Outline each blood parasite and name the species.
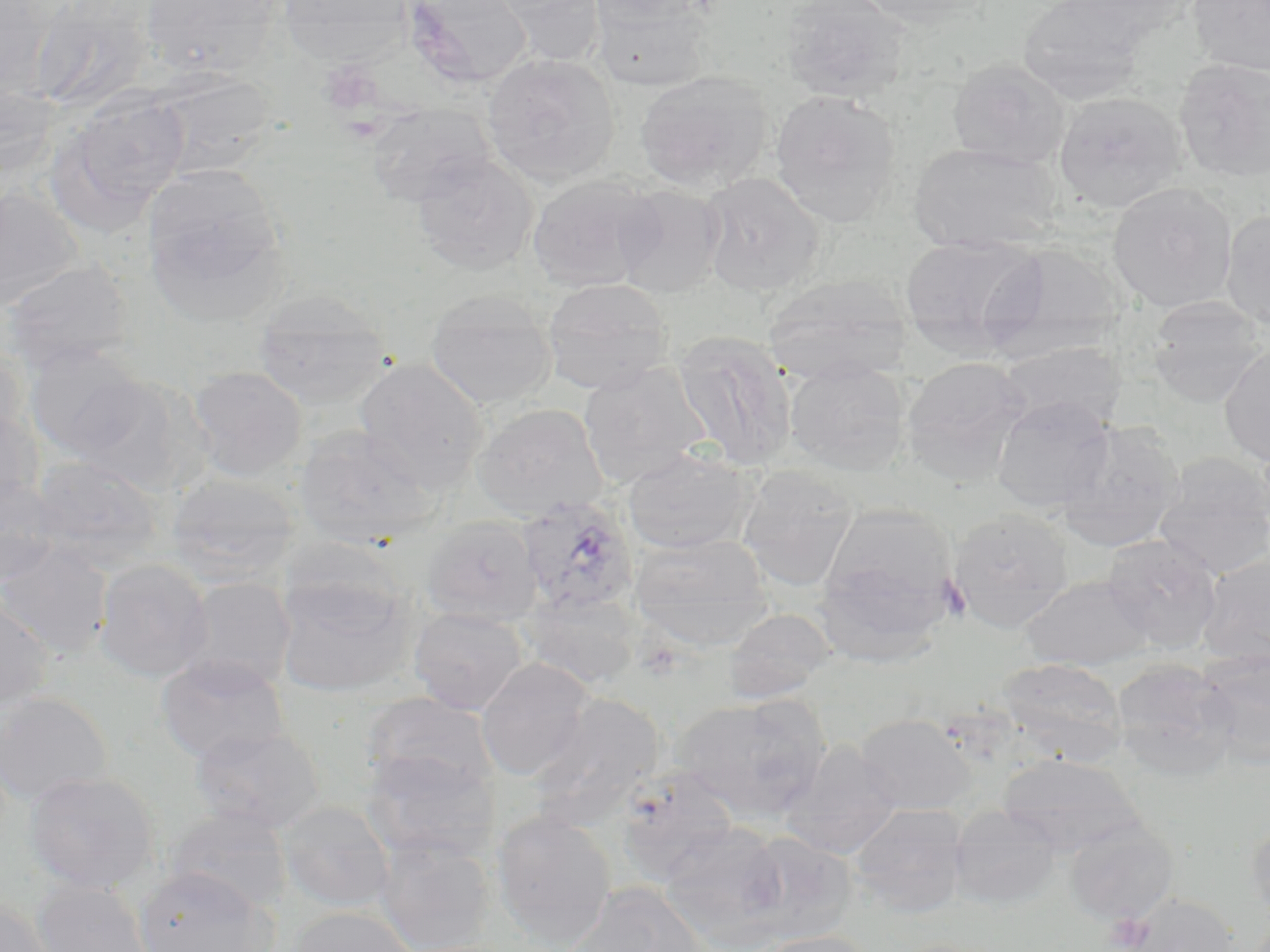

Approximate bounding boxes as named x1/y1/x2/y2 corners in pixels.
Plasmodium ovale-infected red blood cells: (x1=516, y1=496, x2=639, y2=616).
No Plasmodium falciparum, Plasmodium malariae, Plasmodium vivax, Babesia divergens, or Trypanosoma brucei observed.

{
  "slide_level_diagnosis": "Plasmodium ovale",
  "preparation": "thin blood smear",
  "field_of_view": "single",
  "modality": "optical microscopy",
  "image_size": "1270×952 pixels",
  "magnification": "1000x",
  "platelet_locations": "approximate bounding boxes as named x1/y1/x2/y2 corners in pixels: (x1=318, y1=59, x2=383, y2=117), (x1=937, y1=576, x2=972, y2=622), (x1=1104, y1=912, x2=1152, y2=951)",
  "stain": "May-Grünwald-Giemsa",
  "uninfected_red_blood_cell_locations": "approximate bounding boxes as named x1/y1/x2/y2 corners in pixels: (x1=0, y1=0, x2=64, y2=101), (x1=31, y1=0, x2=160, y2=112), (x1=141, y1=0, x2=282, y2=79), (x1=277, y1=0, x2=414, y2=66), (x1=403, y1=0, x2=533, y2=89), (x1=495, y1=0, x2=608, y2=68), (x1=586, y1=0, x2=709, y2=28), (x1=779, y1=0, x2=911, y2=103), (x1=852, y1=0, x2=992, y2=30), (x1=1017, y1=0, x2=1146, y2=104), (x1=1057, y1=0, x2=1197, y2=50), (x1=1187, y1=0, x2=1270, y2=77), (x1=592, y1=2, x2=714, y2=92), (x1=482, y1=53, x2=620, y2=186), (x1=947, y1=57, x2=1071, y2=169), (x1=1173, y1=58, x2=1270, y2=183), (x1=634, y1=69, x2=773, y2=194), (x1=150, y1=72, x2=276, y2=178), (x1=0, y1=78, x2=60, y2=181), (x1=769, y1=89, x2=902, y2=228), (x1=60, y1=91, x2=190, y2=218), (x1=1053, y1=91, x2=1187, y2=213), (x1=365, y1=102, x2=495, y2=207), (x1=908, y1=141, x2=1062, y2=254), (x1=411, y1=152, x2=539, y2=276), (x1=142, y1=163, x2=287, y2=314), (x1=699, y1=172, x2=825, y2=296), (x1=526, y1=175, x2=660, y2=292), (x1=1107, y1=183, x2=1238, y2=313), (x1=612, y1=184, x2=727, y2=297), (x1=0, y1=186, x2=82, y2=308), (x1=1220, y1=209, x2=1270, y2=331), (x1=899, y1=234, x2=1046, y2=352), (x1=983, y1=242, x2=1127, y2=359), (x1=2, y1=259, x2=135, y2=375), (x1=761, y1=274, x2=913, y2=384), (x1=541, y1=278, x2=673, y2=394), (x1=425, y1=289, x2=558, y2=410), (x1=253, y1=291, x2=394, y2=411), (x1=1147, y1=298, x2=1268, y2=407), (x1=672, y1=329, x2=798, y2=472), (x1=0, y1=338, x2=29, y2=452), (x1=996, y1=341, x2=1126, y2=431), (x1=24, y1=342, x2=151, y2=459), (x1=1218, y1=342, x2=1270, y2=467), (x1=901, y1=356, x2=1033, y2=487), (x1=354, y1=357, x2=491, y2=494), (x1=783, y1=360, x2=910, y2=475), (x1=577, y1=361, x2=712, y2=490), (x1=187, y1=365, x2=308, y2=481), (x1=66, y1=376, x2=197, y2=495), (x1=991, y1=395, x2=1116, y2=514), (x1=472, y1=403, x2=608, y2=521), (x1=0, y1=410, x2=43, y2=516), (x1=1057, y1=422, x2=1184, y2=553), (x1=292, y1=425, x2=439, y2=549), (x1=622, y1=447, x2=756, y2=555), (x1=1153, y1=453, x2=1270, y2=579), (x1=30, y1=455, x2=164, y2=569), (x1=735, y1=466, x2=860, y2=592), (x1=165, y1=472, x2=299, y2=587), (x1=0, y1=477, x2=64, y2=587), (x1=947, y1=507, x2=1073, y2=633), (x1=815, y1=510, x2=957, y2=657), (x1=421, y1=515, x2=543, y2=626), (x1=629, y1=533, x2=773, y2=651), (x1=1101, y1=533, x2=1223, y2=653), (x1=0, y1=541, x2=113, y2=658), (x1=1197, y1=553, x2=1270, y2=667), (x1=94, y1=558, x2=214, y2=682), (x1=1020, y1=574, x2=1154, y2=671), (x1=274, y1=575, x2=418, y2=698), (x1=177, y1=577, x2=297, y2=692), (x1=523, y1=590, x2=643, y2=690), (x1=0, y1=594, x2=53, y2=712), (x1=409, y1=606, x2=529, y2=715), (x1=723, y1=608, x2=836, y2=703), (x1=1196, y1=650, x2=1270, y2=768), (x1=155, y1=655, x2=292, y2=763), (x1=476, y1=657, x2=595, y2=781), (x1=996, y1=658, x2=1127, y2=766), (x1=1111, y1=659, x2=1237, y2=781), (x1=0, y1=691, x2=113, y2=807), (x1=362, y1=692, x2=497, y2=800), (x1=528, y1=693, x2=665, y2=827), (x1=674, y1=693, x2=831, y2=823), (x1=855, y1=713, x2=976, y2=814), (x1=190, y1=724, x2=324, y2=834), (x1=780, y1=740, x2=903, y2=860), (x1=361, y1=750, x2=498, y2=863), (x1=996, y1=754, x2=1144, y2=855), (x1=615, y1=767, x2=741, y2=886), (x1=23, y1=772, x2=161, y2=893), (x1=278, y1=801, x2=395, y2=912), (x1=849, y1=802, x2=970, y2=918), (x1=948, y1=805, x2=1062, y2=911), (x1=166, y1=806, x2=292, y2=915), (x1=490, y1=809, x2=617, y2=949), (x1=1245, y1=816, x2=1270, y2=928), (x1=1063, y1=819, x2=1180, y2=925), (x1=659, y1=822, x2=789, y2=944), (x1=736, y1=831, x2=855, y2=943), (x1=374, y1=835, x2=496, y2=952), (x1=134, y1=867, x2=277, y2=952), (x1=31, y1=879, x2=153, y2=952), (x1=563, y1=882, x2=711, y2=952), (x1=1123, y1=893, x2=1241, y2=952), (x1=0, y1=895, x2=55, y2=952), (x1=287, y1=905, x2=421, y2=952), (x1=754, y1=930, x2=879, y2=952)"
}